State the preparation type.
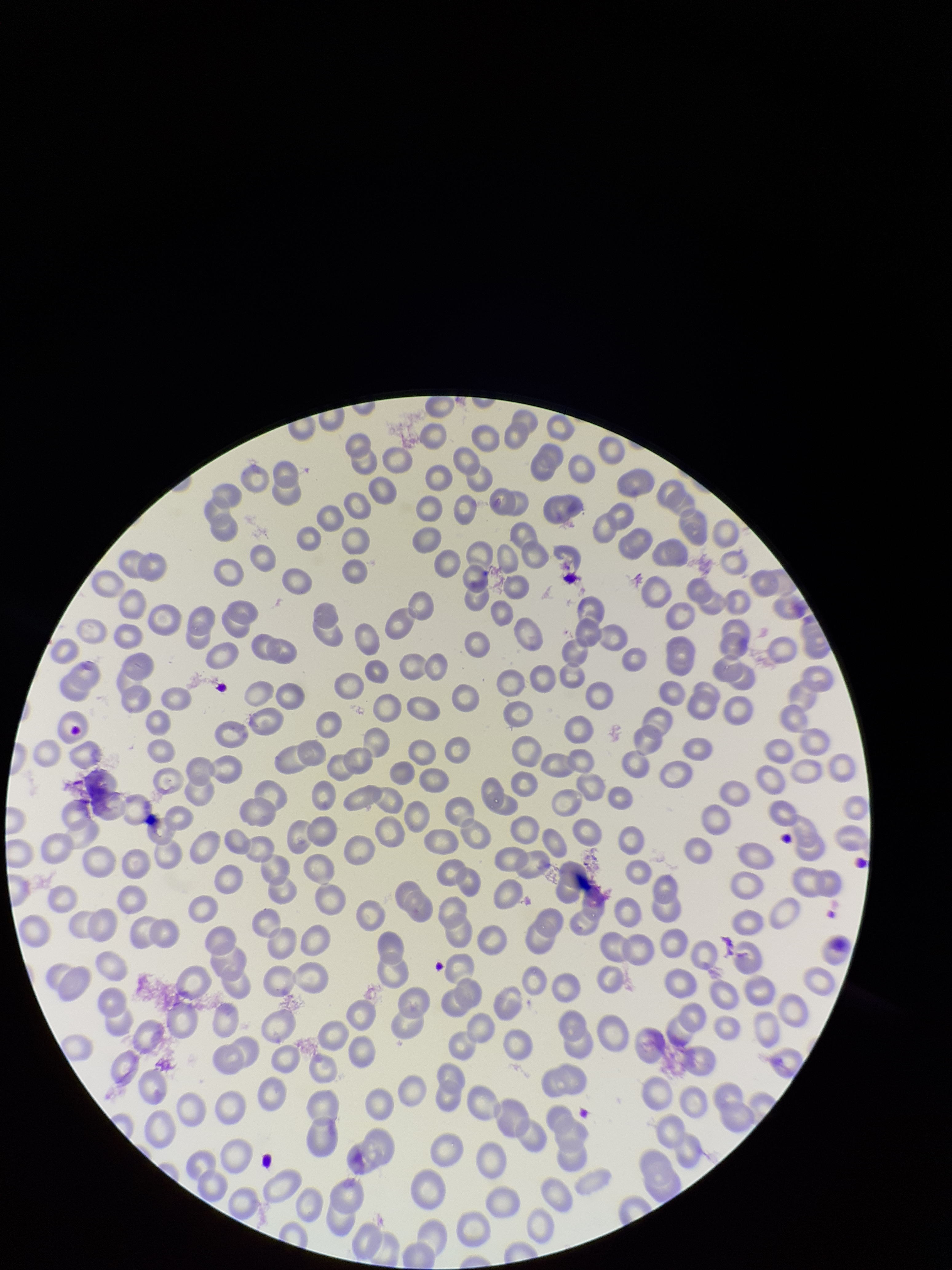
A thin smear.

patient_malaria_status: negative
stain: Giemsa
image_size: 952×1270 pixels
capture: smartphone photograph through the microscope eyepiece
parasitized_red_blood_cells: none detected
red_blood_cell_count: 269
parasitized_red_blood_cell_count: 0
field_of_view: single